Locate every white blood cell.
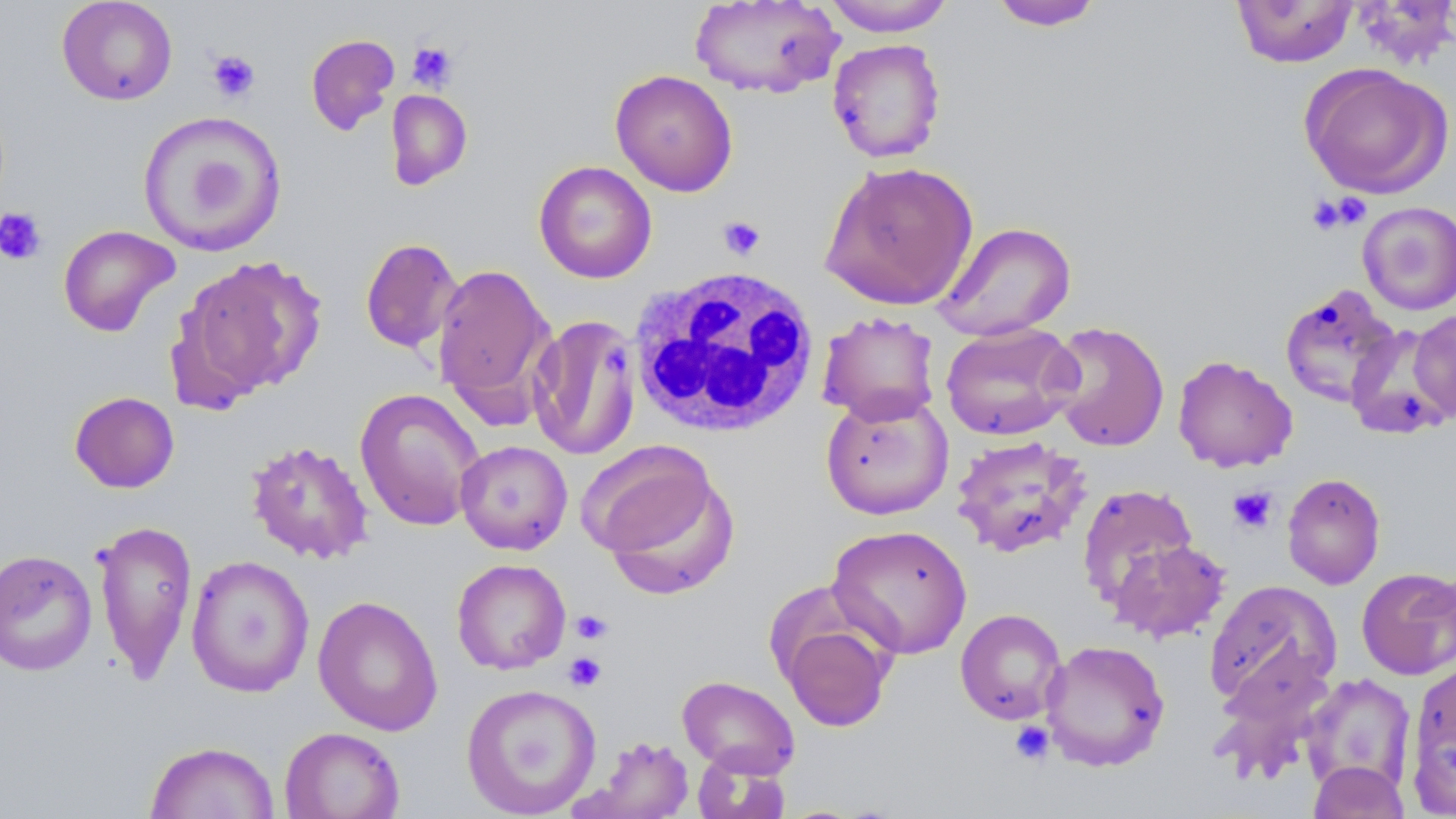
Approximate bounding boxes as named x1/y1/x2/y2 corners in pixels.
White blood cells: (x1=627, y1=266, x2=820, y2=438).

Summary:
  - Platelet locations: (x1=407, y1=41, x2=458, y2=91), (x1=207, y1=50, x2=260, y2=103), (x1=1306, y1=194, x2=1363, y2=235), (x1=0, y1=207, x2=47, y2=265), (x1=718, y1=215, x2=766, y2=261), (x1=602, y1=342, x2=629, y2=372), (x1=1228, y1=485, x2=1278, y2=534), (x1=571, y1=610, x2=613, y2=645), (x1=563, y1=652, x2=607, y2=691), (x1=1009, y1=721, x2=1055, y2=766)
  - Uninfected red blood cell locations: (x1=56, y1=0, x2=178, y2=106), (x1=689, y1=0, x2=843, y2=99), (x1=821, y1=0, x2=956, y2=36), (x1=1231, y1=0, x2=1358, y2=68), (x1=989, y1=1, x2=1105, y2=31), (x1=306, y1=33, x2=400, y2=136), (x1=827, y1=38, x2=947, y2=163), (x1=1299, y1=63, x2=1454, y2=199), (x1=610, y1=69, x2=739, y2=197), (x1=386, y1=89, x2=473, y2=190), (x1=137, y1=110, x2=288, y2=257), (x1=819, y1=159, x2=979, y2=311), (x1=533, y1=160, x2=657, y2=284), (x1=1358, y1=201, x2=1456, y2=316), (x1=932, y1=220, x2=1077, y2=341), (x1=57, y1=224, x2=180, y2=337), (x1=359, y1=237, x2=463, y2=354), (x1=173, y1=254, x2=327, y2=405), (x1=431, y1=263, x2=554, y2=410), (x1=1279, y1=284, x2=1402, y2=408), (x1=1410, y1=308, x2=1456, y2=423), (x1=816, y1=311, x2=941, y2=426), (x1=528, y1=314, x2=642, y2=460), (x1=1045, y1=321, x2=1170, y2=452), (x1=941, y1=323, x2=1080, y2=441), (x1=1344, y1=323, x2=1454, y2=439), (x1=1172, y1=354, x2=1298, y2=473), (x1=354, y1=387, x2=485, y2=532), (x1=69, y1=391, x2=180, y2=493), (x1=820, y1=391, x2=954, y2=520), (x1=950, y1=435, x2=1093, y2=558), (x1=246, y1=439, x2=374, y2=564), (x1=455, y1=440, x2=573, y2=555), (x1=586, y1=444, x2=735, y2=589), (x1=1282, y1=472, x2=1386, y2=590), (x1=1076, y1=483, x2=1198, y2=608), (x1=92, y1=519, x2=198, y2=682), (x1=826, y1=524, x2=973, y2=660), (x1=1108, y1=539, x2=1231, y2=644), (x1=0, y1=549, x2=98, y2=676), (x1=185, y1=555, x2=315, y2=697), (x1=451, y1=558, x2=571, y2=674), (x1=1356, y1=567, x2=1456, y2=680), (x1=1203, y1=579, x2=1342, y2=713), (x1=312, y1=595, x2=444, y2=736), (x1=954, y1=608, x2=1067, y2=725), (x1=781, y1=620, x2=893, y2=732), (x1=1040, y1=639, x2=1170, y2=771), (x1=1210, y1=653, x2=1337, y2=783), (x1=1405, y1=659, x2=1456, y2=813), (x1=1300, y1=673, x2=1417, y2=795), (x1=677, y1=675, x2=801, y2=778), (x1=460, y1=682, x2=601, y2=817), (x1=279, y1=726, x2=405, y2=819), (x1=576, y1=735, x2=696, y2=818), (x1=144, y1=741, x2=280, y2=819), (x1=691, y1=749, x2=790, y2=819), (x1=1307, y1=761, x2=1411, y2=819)
  - Slide-level diagnosis: no evidence of blood parasites
  - Stain: May-Grünwald-Giemsa
  - Modality: light microscopy
  - Image size: 1456×819 pixels
  - Field of view: one of a larger specimen
  - Preparation: thin blood smear
  - Magnification: 1000x